Name the parasite shown.
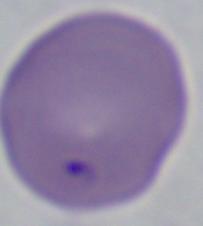
This is Babesia.

{
  "magnification": "1000x",
  "modality": "photomicrograph"
}